Identify the parasite.
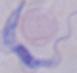
This is a trypanosome.

modality = photomicrograph
magnification = 1000x